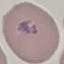

Result: malaria parasites identified. Cell patch, automatically extracted from a larger field of view and resized to 64 × 64 pixels. Thin blood smear. Acquired by smartphone through the microscope eyepiece. Giemsa stain.